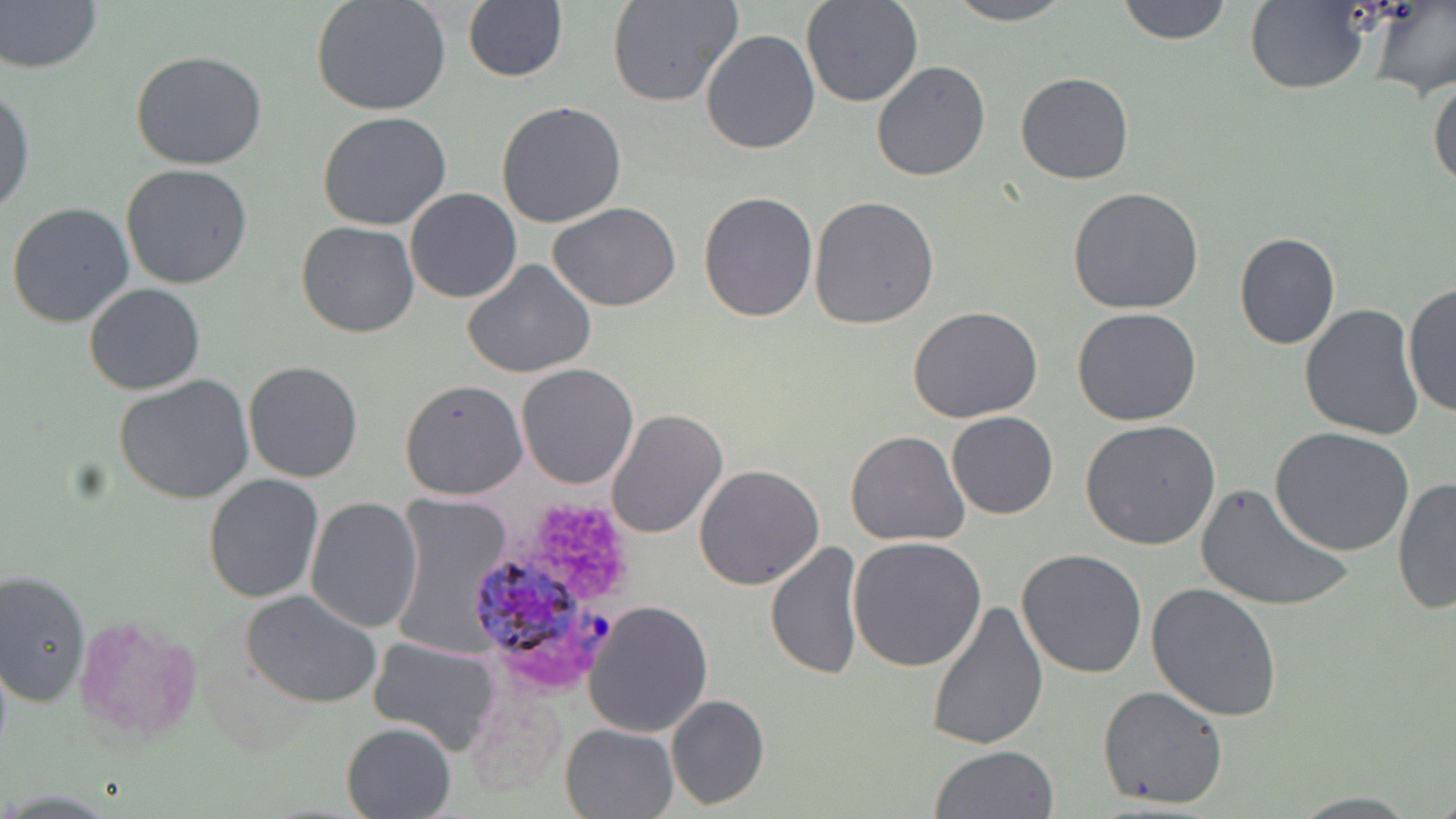
Summary:
  - Coordinate format: approximate bounding boxes as [x1, y1, x2, y2] in pixels
  - Uninfected red blood cell locations: [311, 0, 452, 117], [605, 0, 743, 107], [800, 0, 924, 108], [941, 0, 1079, 25], [1114, 0, 1234, 46], [1366, 0, 1456, 100], [1, 2, 102, 75], [462, 2, 566, 82], [1245, 2, 1368, 94], [701, 28, 819, 154], [131, 52, 268, 171], [871, 61, 991, 181], [1427, 70, 1456, 191], [1015, 72, 1136, 185], [0, 81, 36, 217], [496, 100, 627, 229], [317, 110, 452, 231], [121, 163, 254, 289], [405, 188, 522, 304], [1066, 188, 1206, 315], [697, 191, 818, 323], [808, 196, 939, 329], [6, 202, 135, 330], [548, 203, 680, 312], [296, 220, 420, 337], [1234, 233, 1341, 350], [463, 258, 597, 379], [1403, 281, 1455, 420], [83, 283, 206, 396], [1299, 304, 1424, 441], [908, 308, 1043, 424], [1072, 308, 1202, 427], [242, 361, 364, 482], [516, 362, 639, 488], [114, 374, 256, 505], [399, 378, 527, 498], [606, 409, 729, 540], [947, 411, 1058, 520], [1081, 420, 1222, 550], [1270, 426, 1416, 557], [844, 430, 969, 546], [693, 464, 825, 590], [203, 474, 325, 605], [1393, 475, 1456, 617], [1192, 482, 1357, 615], [304, 495, 422, 633], [390, 496, 517, 652], [848, 537, 988, 671], [764, 541, 866, 680], [1017, 550, 1148, 679], [0, 570, 91, 706], [1146, 583, 1283, 722], [243, 590, 382, 708], [927, 595, 1048, 752], [583, 599, 714, 740], [69, 612, 200, 746], [366, 635, 500, 754], [464, 675, 568, 802], [1097, 684, 1228, 810], [665, 694, 770, 809], [339, 722, 457, 818], [559, 722, 680, 817], [929, 744, 1059, 819], [1284, 791, 1424, 817]
  - Plasmodium ovale-infected red blood cell locations: [471, 556, 619, 698]
  - Platelet locations: [533, 504, 629, 601]
  - Slide-level diagnosis: Plasmodium ovale
  - Modality: optical microscopy
  - Stain: May-Grünwald-Giemsa
  - Magnification: 1000x
  - Image size: 1456×819 pixels
  - Preparation: thin blood smear
  - Field of view: single